Outline each Plasmodium falciparum-infected red blood cell.
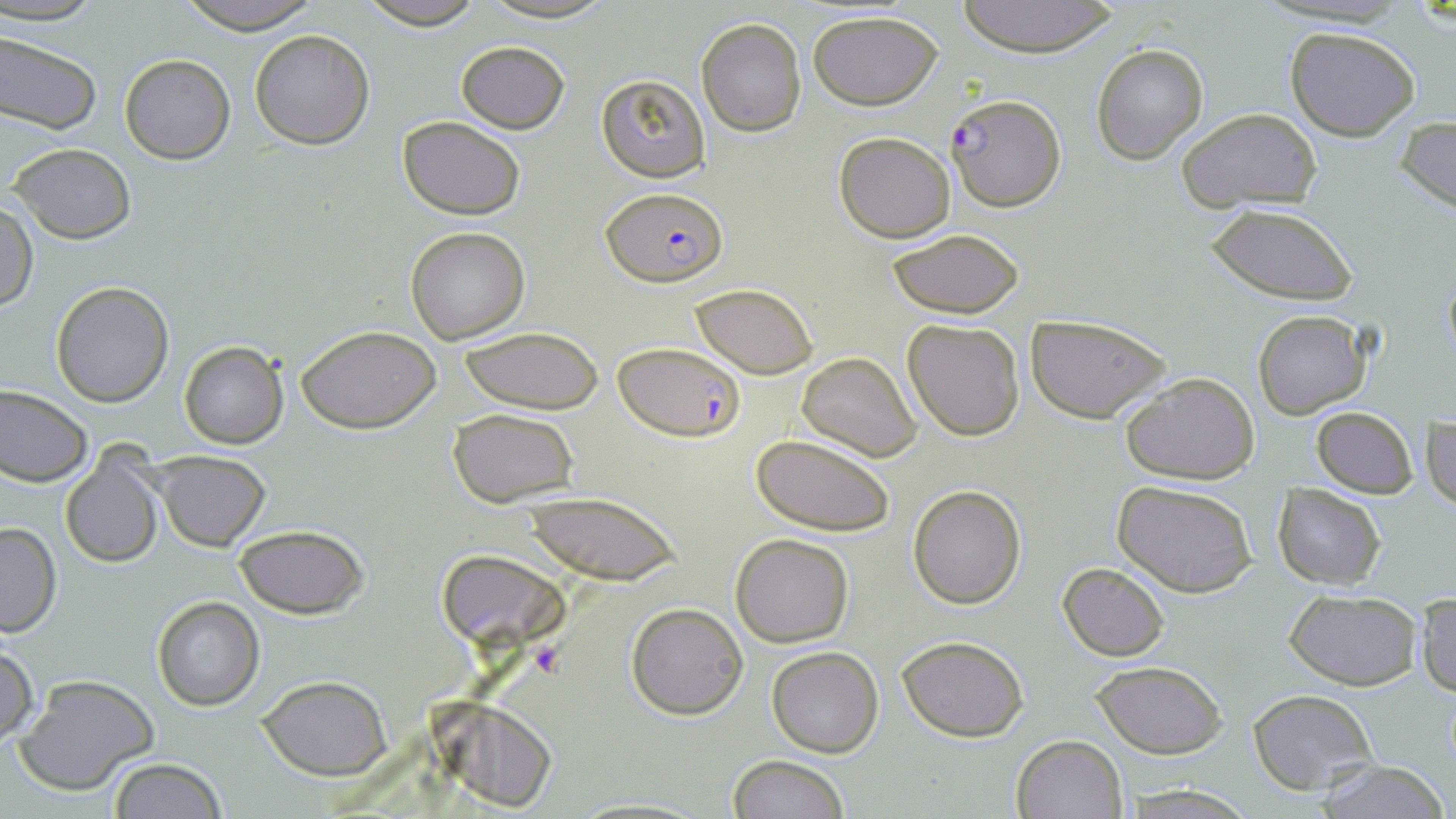

Approximate bounding boxes as [x1, y1, x2, y2] in pixels.
Plasmodium falciparum-infected red blood cells: [944, 92, 1068, 212], [602, 188, 726, 286], [616, 342, 744, 439].

Summary:
  - Uninfected red blood cell locations: [0, 0, 109, 26], [171, 0, 324, 32], [355, 0, 487, 29], [477, 0, 619, 24], [955, 0, 1121, 57], [807, 9, 943, 110], [696, 18, 806, 137], [1285, 25, 1420, 140], [250, 29, 375, 149], [0, 31, 102, 134], [456, 40, 570, 134], [1091, 43, 1207, 163], [118, 54, 236, 165], [595, 74, 709, 184], [1176, 108, 1323, 211], [396, 115, 525, 221], [1397, 115, 1456, 215], [833, 131, 958, 242], [8, 143, 137, 244], [1, 198, 37, 313], [1205, 203, 1358, 305], [405, 227, 531, 345], [887, 228, 1023, 319], [1441, 267, 1456, 370], [51, 281, 174, 407], [692, 283, 817, 378], [1253, 311, 1372, 421], [1025, 313, 1172, 423], [902, 318, 1026, 440], [296, 324, 443, 433], [459, 328, 604, 414], [179, 341, 288, 449], [798, 351, 921, 460], [1120, 370, 1260, 486], [0, 384, 91, 486], [1312, 405, 1417, 497], [447, 408, 580, 509], [1423, 409, 1456, 516], [750, 434, 895, 536], [152, 450, 272, 551], [60, 452, 167, 568], [1114, 479, 1258, 597], [1272, 483, 1387, 590], [908, 484, 1027, 609], [525, 492, 681, 584], [0, 523, 61, 637], [234, 524, 369, 618], [731, 533, 854, 646], [436, 548, 560, 648], [1057, 562, 1169, 661], [1283, 588, 1423, 692], [1414, 591, 1456, 698], [151, 595, 265, 711], [625, 603, 748, 719], [898, 636, 1028, 741], [0, 645, 38, 746], [767, 646, 884, 758], [1090, 660, 1228, 759], [15, 675, 160, 795], [256, 675, 394, 780], [1248, 689, 1379, 795], [1010, 735, 1128, 819], [728, 754, 851, 819], [107, 757, 228, 819], [1313, 759, 1450, 819], [1122, 783, 1256, 817]
  - Platelet locations: [529, 641, 568, 678]
  - Slide-level diagnosis: Plasmodium falciparum
  - Image size: 1456×819 pixels
  - Magnification: 1000x
  - Field of view: one of a larger specimen
  - Preparation: thin blood film
  - Modality: light microscopy
  - Stain: May-Grünwald-Giemsa